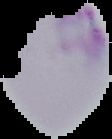
From a thin blood film. Image is 112×139 pixels. Result: no Plasmodium parasites detected. Cell region segmented out of the field of view; the surrounding area is masked to black.